Outline each blood parasite and name the species.
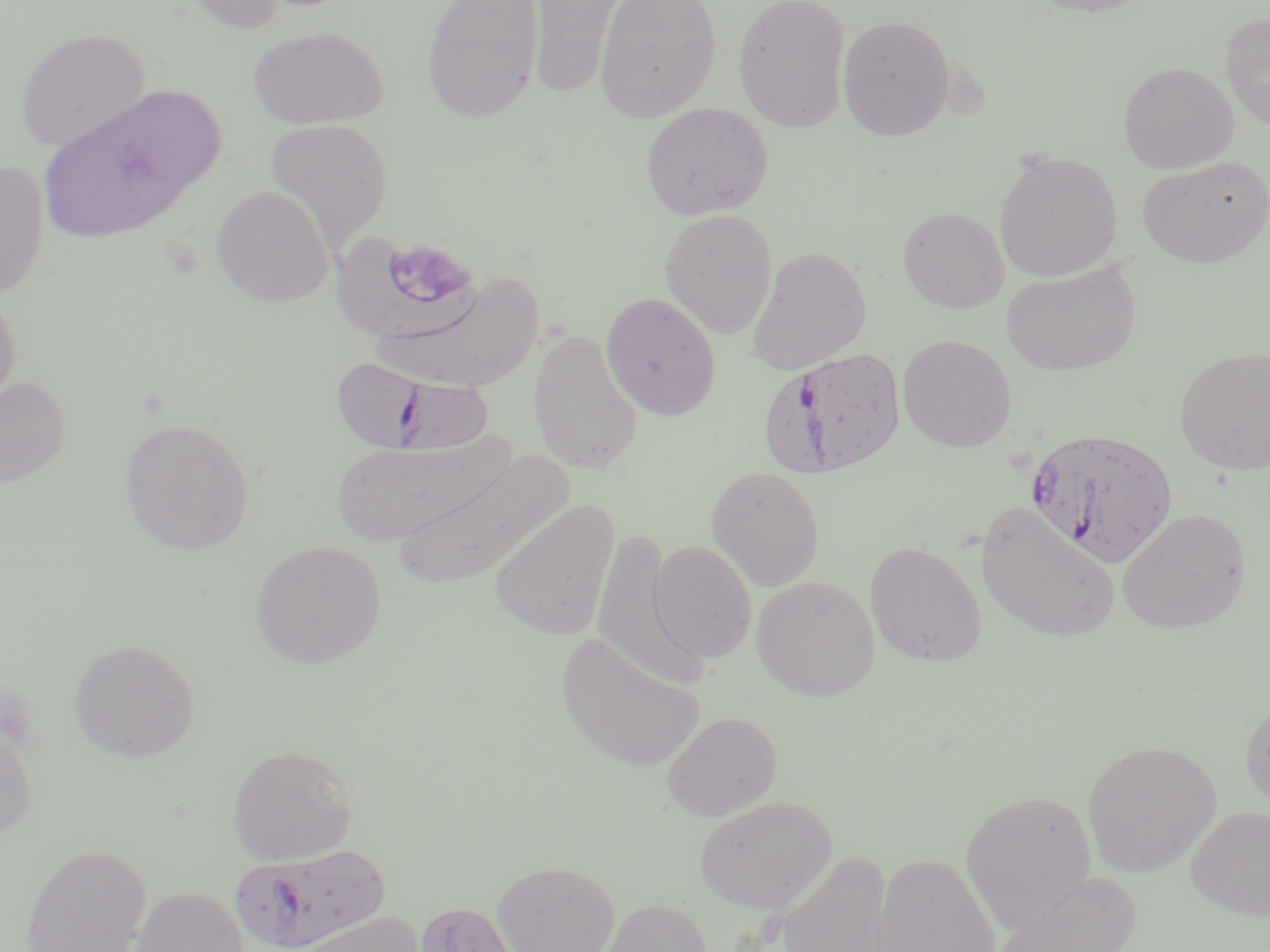
Approximate bounding boxes as [x1, y1, x2, y2] in pixels.
Plasmodium falciparum-infected red blood cells: [760, 346, 909, 478], [328, 358, 500, 458], [1026, 426, 1178, 567], [230, 843, 391, 952].
No Plasmodium ovale, Plasmodium malariae, Plasmodium vivax, Babesia divergens, or Trypanosoma brucei observed.

Summary:
  - Uninfected red blood cell locations: [174, 0, 290, 34], [422, 0, 544, 123], [527, 0, 626, 100], [593, 0, 721, 122], [733, 0, 852, 133], [1023, 0, 1158, 17], [1220, 12, 1270, 131], [837, 15, 955, 141], [248, 26, 387, 129], [15, 27, 151, 152], [1118, 61, 1239, 174], [36, 83, 223, 245], [640, 102, 772, 220], [264, 118, 393, 256], [994, 151, 1123, 282], [1137, 156, 1270, 267], [0, 159, 50, 300], [211, 185, 333, 306], [898, 206, 1010, 313], [659, 209, 777, 339], [332, 235, 487, 347], [746, 245, 872, 375], [1000, 260, 1142, 376], [370, 274, 545, 395], [0, 288, 21, 416], [600, 292, 721, 421], [528, 329, 644, 476], [897, 334, 1017, 452], [1174, 347, 1269, 474], [0, 376, 71, 490], [119, 416, 255, 556], [327, 433, 516, 545], [388, 449, 570, 592], [705, 466, 825, 591], [488, 500, 620, 642], [974, 502, 1121, 645], [1117, 507, 1252, 634], [589, 527, 704, 691], [647, 539, 757, 664], [250, 540, 387, 669], [864, 541, 987, 667], [751, 575, 880, 700], [555, 632, 705, 773], [68, 639, 200, 762], [1240, 695, 1270, 813], [662, 711, 782, 821], [0, 715, 37, 845], [1081, 739, 1223, 877], [227, 743, 358, 865], [960, 787, 1097, 933], [693, 794, 837, 914], [1186, 805, 1270, 920], [20, 844, 152, 952], [774, 850, 894, 952], [871, 852, 1001, 952], [493, 860, 619, 952], [993, 870, 1142, 951], [128, 885, 250, 952], [596, 898, 712, 951], [413, 900, 523, 952], [290, 910, 425, 952]
  - Platelet locations: [392, 244, 472, 302]
  - Slide-level diagnosis: Plasmodium falciparum
  - Field of view: one of a larger specimen
  - Preparation: thin blood smear
  - Magnification: 1000x
  - Modality: light microscopy
  - Image size: 1270×952 pixels
  - Stain: May-Grünwald-Giemsa